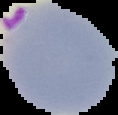
Summary:
  - Image type: segmented cell region with the area outside set to black
  - Preparation: thin blood smear
  - Image size: 118×115 pixels
  - Malaria status: parasitized